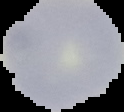

preparation = thin blood smear
image type = cell region segmented out of the field of view; surrounding area masked to black
result = negative for malaria parasites
image size = 124×112 pixels